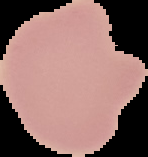

Summary:
  - Preparation: thin blood film
  - Result: negative for malaria parasites
  - Image size: 148×157 pixels
  - Image type: cell region segmented out of the field of view; surrounding area masked to black